Point out each Plasmodium parasite.
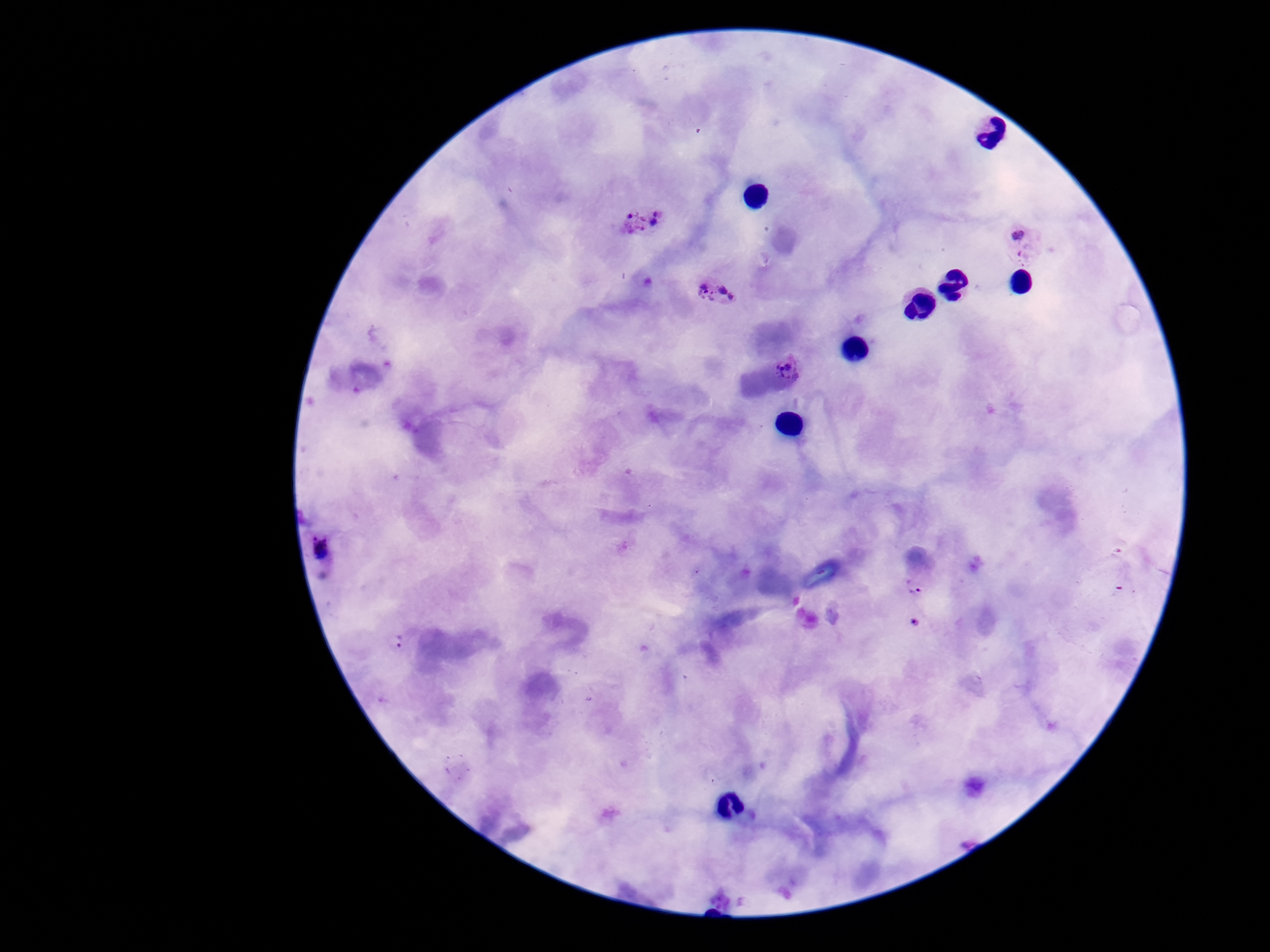

Approximate centers as {x, y} in pixels.
Plasmodium parasites: {642, 222}, {1027, 244}, {716, 293}, {788, 367}, {325, 549}, {918, 585}, {915, 624}, {397, 644}.

capture = smartphone camera through the microscope eyepiece
patient malaria status = infected
magnification = 100x
stain = Giemsa
image size = 1270×952 pixels
field of view = one from this slide
preparation = thick peripheral-blood smear